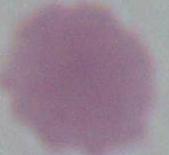

1000x magnification. Micrograph. An erythrocyte is shown.